Name the parasite shown.
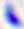

This is Toxoplasma gondii.

Summary:
  - Magnification: 400x
  - Modality: photomicrograph